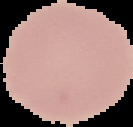

preparation: thin blood smear
image_type: cell region segmented out of the field of view; surrounding area masked to black
malaria_status: uninfected
image_size: 133×127 pixels